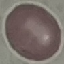

result: no malaria parasites detected
image_type: automatically extracted cell patch, resized to 64 × 64 pixels
preparation: thin blood film
stain: Giemsa
capture: smartphone camera at the microscope eyepiece